Comment on the morphology of the red blood cells.
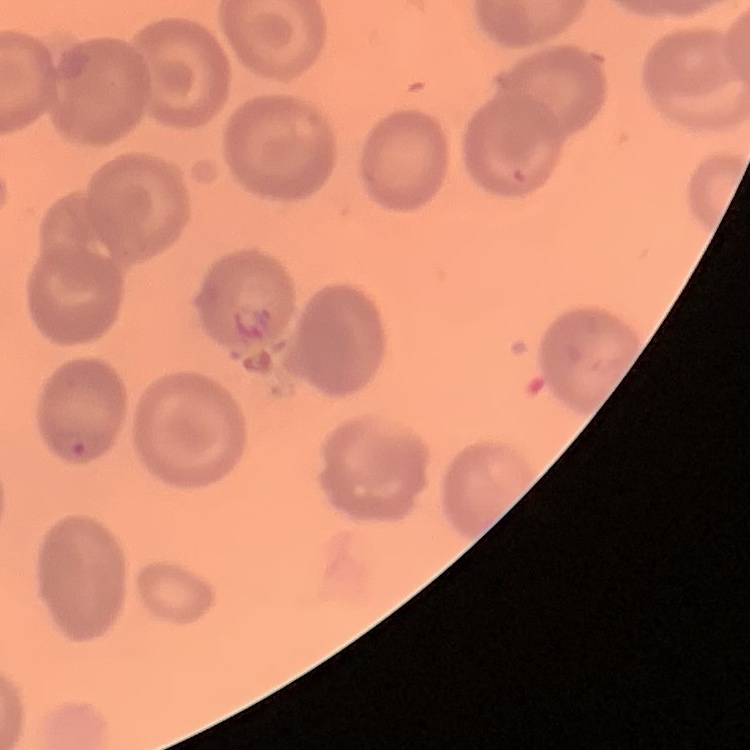

No rouleaux formation.

Stained with either Field's or Giemsa. Thin blood film. One tile cut from a larger photomicrograph.